Point out every Plasmodium parasite and every leukocyte.
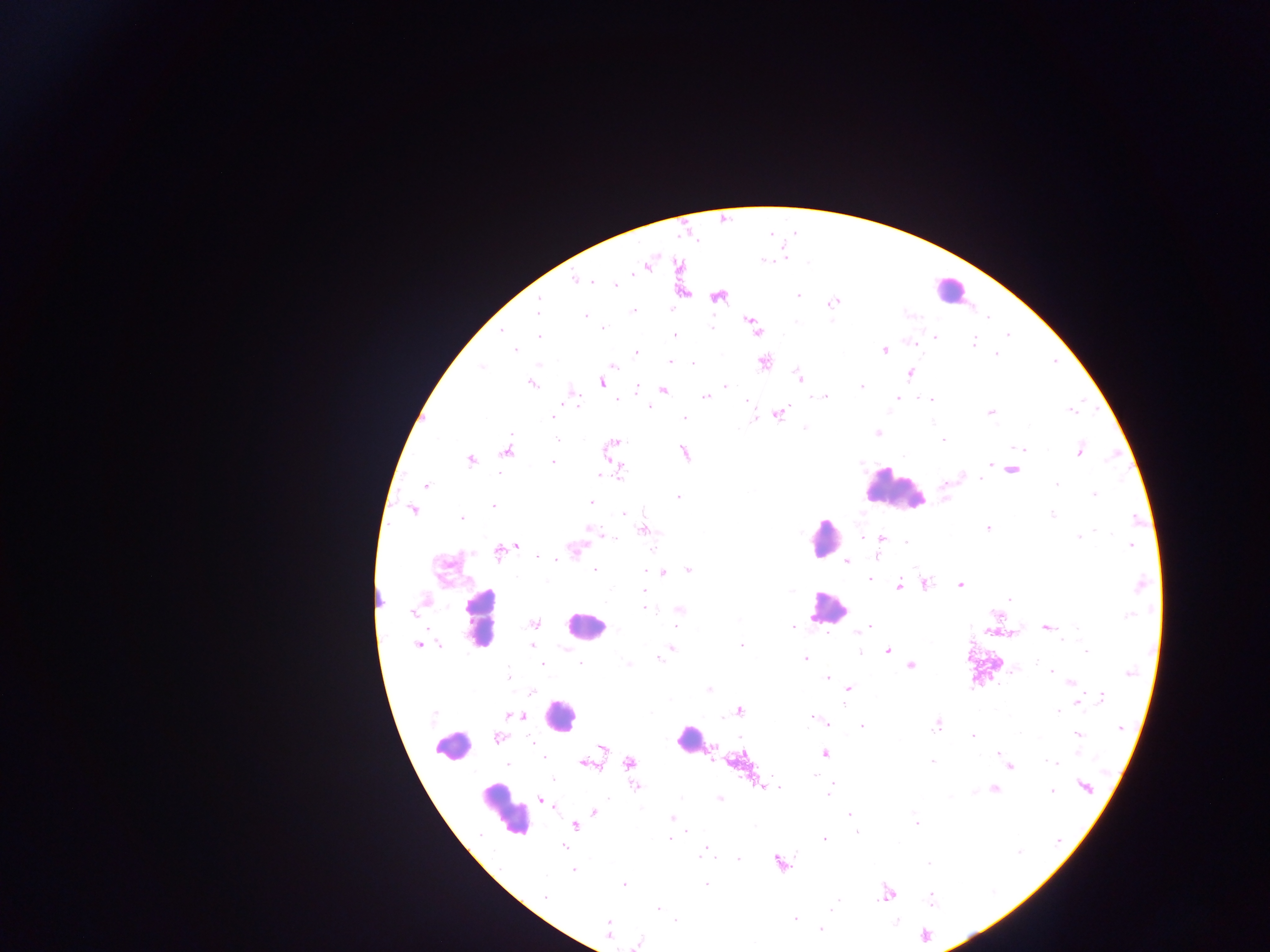
Approximate centers as [x, y] in pixels.
Plasmodium parasites: [784, 258], [764, 260], [634, 271], [575, 279], [592, 282], [614, 285], [798, 294], [718, 296], [538, 303], [833, 303], [537, 310], [633, 310], [585, 316], [752, 322], [710, 327], [603, 328], [756, 329], [501, 331], [675, 335], [1008, 335], [539, 337], [935, 337], [973, 342], [515, 350], [884, 350], [637, 353], [996, 354], [764, 361], [670, 362], [693, 364], [613, 366], [482, 367], [909, 374], [800, 378], [602, 382], [531, 384], [861, 386], [726, 387], [637, 389], [663, 390], [706, 396], [825, 397], [898, 398], [617, 400], [930, 400], [576, 401], [1071, 411], [991, 412], [779, 414], [754, 416], [553, 417], [684, 418], [804, 428], [877, 433], [555, 438], [942, 439], [613, 444], [1021, 449], [507, 451], [1079, 451], [684, 453], [471, 460], [553, 462], [991, 465], [1012, 470], [619, 472], [601, 475], [981, 479], [1056, 484], [426, 485], [1094, 495], [679, 497], [590, 502], [493, 506], [414, 510], [625, 514], [1052, 514], [462, 518], [1136, 520], [987, 528], [644, 530], [1095, 531], [596, 532], [609, 536], [862, 536], [1079, 537], [881, 538], [906, 541], [516, 545], [1131, 545], [575, 549], [499, 552], [877, 555], [537, 556], [846, 561], [595, 570], [689, 570], [645, 571], [663, 573], [869, 579], [925, 584], [960, 585], [1141, 585], [899, 586], [644, 591], [1010, 600], [644, 608], [679, 610], [413, 612], [995, 614], [1128, 615], [535, 624], [869, 626], [793, 627], [1046, 628], [990, 629], [854, 631], [1013, 631], [1062, 641], [418, 645], [532, 645], [742, 645], [672, 647], [887, 651], [1086, 651], [860, 652], [658, 659], [805, 659], [1037, 660], [542, 664], [581, 664], [629, 665], [910, 666], [1014, 669], [1052, 672], [1129, 673], [507, 674], [827, 677], [1072, 683], [849, 688], [709, 689], [531, 692], [1075, 695], [1102, 698], [843, 703], [1078, 703], [739, 710], [1058, 712], [515, 716], [813, 718], [826, 723], [936, 725], [861, 727], [1120, 728], [1020, 732], [1077, 734], [972, 735], [498, 738], [601, 747], [1078, 753], [824, 754], [998, 754], [543, 756], [1001, 757], [932, 761], [1050, 761], [630, 763], [586, 764], [507, 765], [1011, 767], [813, 774], [552, 780], [636, 786], [1085, 786], [764, 787], [994, 789], [1052, 791], [973, 792], [828, 794], [719, 798], [541, 799], [547, 803], [594, 812], [849, 815], [672, 818], [916, 824], [574, 826], [686, 832], [857, 832], [669, 838], [824, 839], [1059, 839], [564, 846], [706, 846], [704, 852], [1018, 852], [738, 859], [780, 863], [929, 864], [573, 870], [623, 884], [707, 884], [886, 894], [545, 896], [930, 899], [832, 908], [658, 909], [795, 918], [676, 921], [896, 922], [608, 924], [820, 930], [925, 935], [639, 942].
Leukocytes: [948, 289], [895, 492], [823, 538], [377, 597], [827, 607], [481, 621], [584, 627], [560, 716], [452, 745], [693, 745], [504, 810].

Summary:
  - Capture: mobile-phone photograph through a microscope
  - Country: Ghana
  - Preparation: thick blood smear
  - Image size: 1270×952 pixels
  - Field of view: single